Outline each blood parasite and name the species.
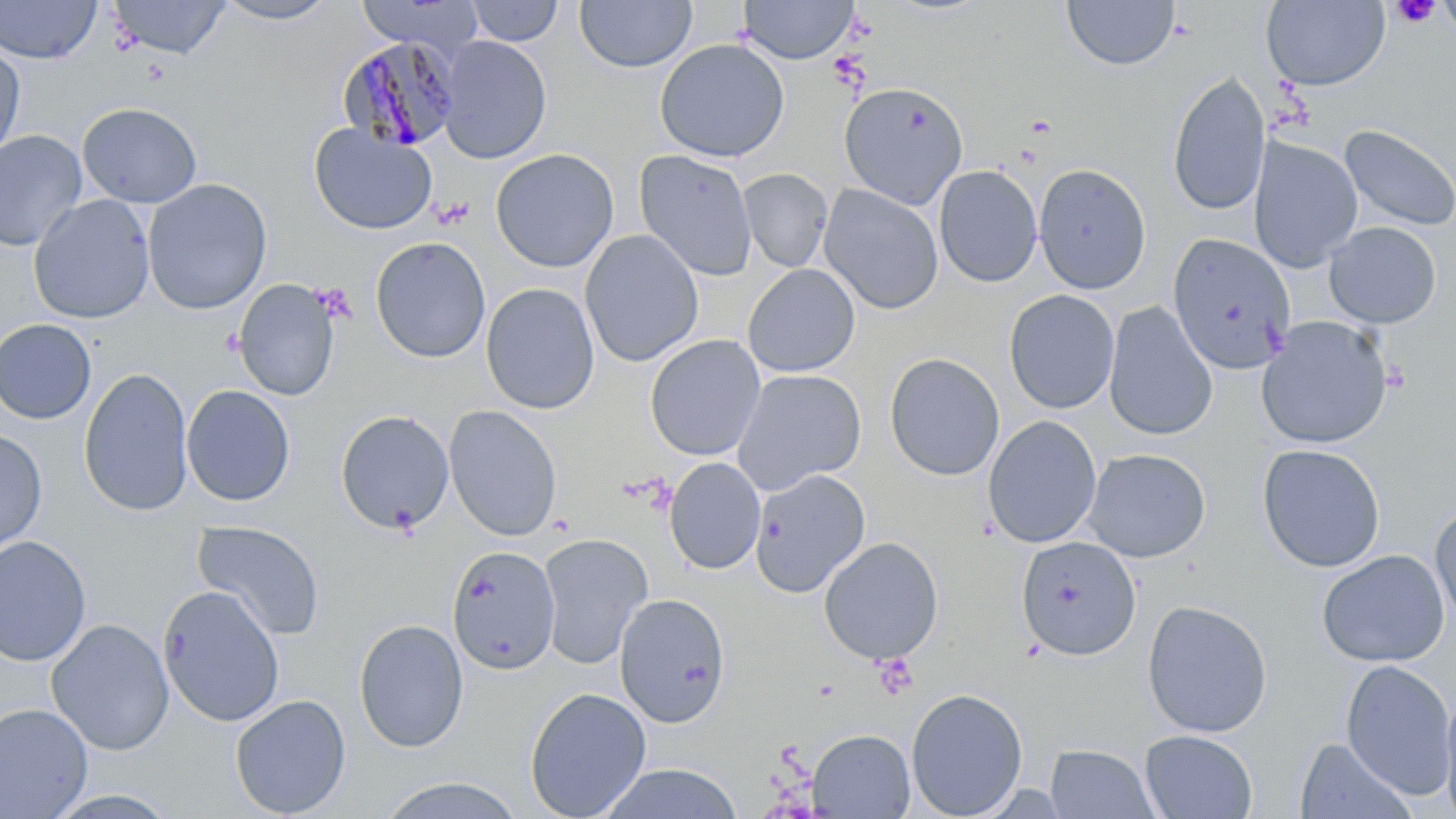
Approximate bounding boxes as named x1/y1/x2/y2 corners in pixels.
Plasmodium malariae-infected red blood cells: (x1=338, y1=36, x2=462, y2=153).
No Plasmodium falciparum, Plasmodium ovale, Plasmodium vivax, Babesia divergens, or Trypanosoma brucei observed.

slide-level diagnosis = Plasmodium malariae
preparation = thin blood smear
platelet locations = approximate bounding boxes as named x1/y1/x2/y2 corners in pixels: (x1=1391, y1=0, x2=1441, y2=29), (x1=1381, y1=360, x2=1411, y2=393), (x1=872, y1=653, x2=917, y2=698)
modality = light microscopy
stain = May-Grünwald-Giemsa
field of view = one of a larger specimen
image size = 1456×819 pixels
magnification = 1000x
uninfected red blood cell locations = approximate bounding boxes as named x1/y1/x2/y2 corners in pixels: (x1=0, y1=0, x2=102, y2=64), (x1=109, y1=0, x2=232, y2=60), (x1=213, y1=0, x2=341, y2=25), (x1=575, y1=0, x2=697, y2=73), (x1=739, y1=0, x2=858, y2=64), (x1=1062, y1=0, x2=1180, y2=71), (x1=1261, y1=0, x2=1391, y2=92), (x1=1439, y1=0, x2=1456, y2=40), (x1=356, y1=1, x2=486, y2=54), (x1=465, y1=1, x2=565, y2=46), (x1=437, y1=35, x2=552, y2=164), (x1=654, y1=38, x2=790, y2=162), (x1=0, y1=41, x2=25, y2=163), (x1=1167, y1=71, x2=1271, y2=217), (x1=839, y1=81, x2=968, y2=208), (x1=77, y1=102, x2=202, y2=208), (x1=308, y1=123, x2=437, y2=236), (x1=1339, y1=124, x2=1455, y2=233), (x1=0, y1=130, x2=87, y2=251), (x1=1247, y1=137, x2=1363, y2=272), (x1=490, y1=148, x2=619, y2=273), (x1=634, y1=150, x2=758, y2=281), (x1=1033, y1=163, x2=1151, y2=294), (x1=933, y1=165, x2=1043, y2=287), (x1=738, y1=168, x2=834, y2=273), (x1=142, y1=178, x2=272, y2=315), (x1=818, y1=183, x2=944, y2=314), (x1=28, y1=194, x2=155, y2=324), (x1=1323, y1=221, x2=1441, y2=328), (x1=580, y1=229, x2=704, y2=367), (x1=1168, y1=232, x2=1297, y2=375), (x1=370, y1=237, x2=491, y2=363), (x1=742, y1=263, x2=861, y2=378), (x1=233, y1=279, x2=340, y2=401), (x1=481, y1=283, x2=600, y2=415), (x1=1003, y1=289, x2=1120, y2=414), (x1=1103, y1=302, x2=1217, y2=441), (x1=1256, y1=316, x2=1393, y2=449), (x1=0, y1=318, x2=97, y2=424), (x1=645, y1=334, x2=766, y2=461), (x1=884, y1=352, x2=1005, y2=481), (x1=79, y1=367, x2=194, y2=516), (x1=731, y1=368, x2=867, y2=494), (x1=182, y1=385, x2=295, y2=506), (x1=443, y1=405, x2=562, y2=541), (x1=335, y1=409, x2=454, y2=534), (x1=983, y1=415, x2=1102, y2=548), (x1=0, y1=428, x2=46, y2=553), (x1=1256, y1=443, x2=1386, y2=573), (x1=1082, y1=448, x2=1211, y2=563), (x1=664, y1=457, x2=766, y2=574), (x1=750, y1=468, x2=870, y2=598), (x1=1429, y1=501, x2=1456, y2=631), (x1=192, y1=520, x2=325, y2=641), (x1=537, y1=532, x2=652, y2=670), (x1=0, y1=535, x2=92, y2=666), (x1=818, y1=536, x2=944, y2=665), (x1=1015, y1=536, x2=1142, y2=660), (x1=446, y1=545, x2=561, y2=674), (x1=1317, y1=549, x2=1450, y2=668), (x1=157, y1=584, x2=286, y2=727), (x1=613, y1=593, x2=731, y2=727), (x1=1141, y1=599, x2=1273, y2=738), (x1=46, y1=618, x2=174, y2=756), (x1=353, y1=618, x2=469, y2=753), (x1=1339, y1=659, x2=1456, y2=800), (x1=1440, y1=683, x2=1456, y2=819), (x1=524, y1=687, x2=652, y2=819), (x1=905, y1=688, x2=1028, y2=819), (x1=229, y1=694, x2=351, y2=817), (x1=0, y1=703, x2=93, y2=819), (x1=808, y1=729, x2=915, y2=818), (x1=1139, y1=730, x2=1258, y2=818), (x1=1294, y1=737, x2=1416, y2=819), (x1=1045, y1=743, x2=1159, y2=818), (x1=596, y1=763, x2=745, y2=819), (x1=372, y1=775, x2=531, y2=819), (x1=43, y1=789, x2=181, y2=818)